Report the malaria status of this cell.
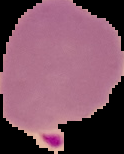

Parasitized.

Summary:
  - Image type: segmented cell region on a black background
  - Image size: 124×154 pixels
  - Preparation: thin blood smear